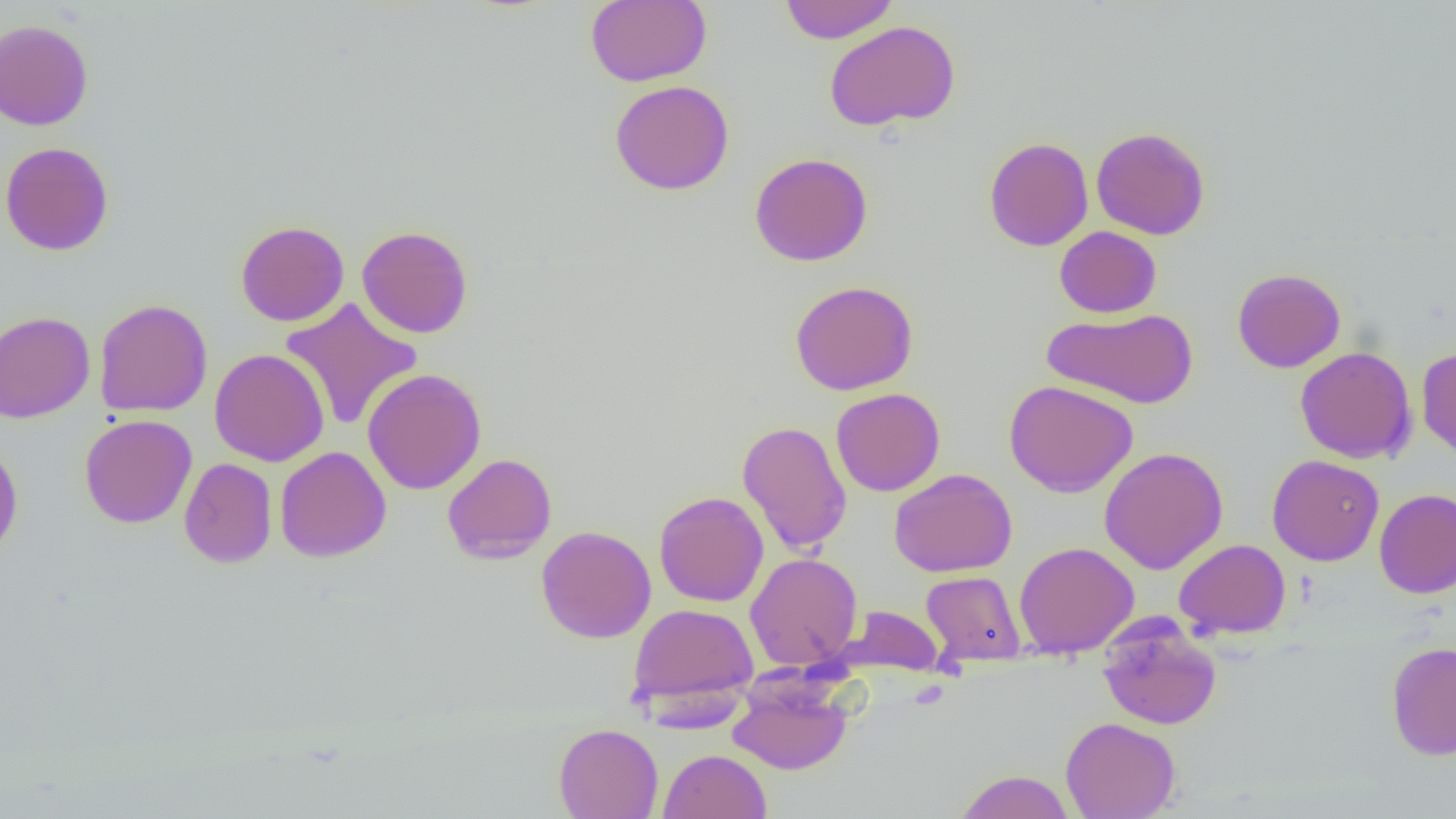 Approximate bounding boxes as [x1, y1, x2, y2] in pixels. Uninfected red blood cell locations: [584, 0, 712, 87], [779, 0, 899, 44], [0, 18, 94, 131], [823, 20, 961, 132], [610, 80, 735, 196], [1090, 126, 1211, 240], [983, 136, 1093, 251], [0, 141, 114, 256], [750, 152, 873, 266], [235, 220, 349, 327], [357, 225, 473, 338], [1054, 226, 1162, 317], [1232, 268, 1345, 373], [790, 280, 919, 396], [94, 298, 213, 417], [279, 298, 423, 431], [1042, 308, 1198, 409], [0, 310, 95, 423], [1295, 346, 1417, 464], [1417, 346, 1456, 462], [210, 348, 330, 467], [363, 368, 487, 494], [1004, 380, 1138, 497], [831, 388, 945, 496], [79, 414, 197, 529], [737, 420, 852, 555], [0, 440, 24, 560], [275, 446, 391, 562], [1099, 447, 1228, 574], [442, 453, 557, 564], [1267, 454, 1384, 566], [179, 457, 277, 568], [889, 468, 1017, 577], [1374, 488, 1456, 599], [653, 491, 768, 607], [535, 525, 656, 643], [1174, 539, 1291, 639], [1013, 541, 1140, 658], [745, 553, 863, 670], [921, 570, 1025, 665], [628, 602, 759, 711], [839, 605, 944, 675], [1097, 615, 1222, 730], [1386, 641, 1456, 760], [728, 679, 852, 775], [1060, 716, 1180, 819], [553, 723, 663, 819], [658, 749, 771, 819], [952, 770, 1077, 818]. Slide-level diagnosis: no evidence of blood parasites. Captured at 1000x magnification. Image is 1456×819 pixels. Thin blood smear. One field of a larger specimen. Light microscopy.